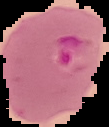
Malaria status: parasitized. Cell region segmented out of the field of view; the surrounding area is masked to black. From a thin blood smear. Image is 109×127 pixels.